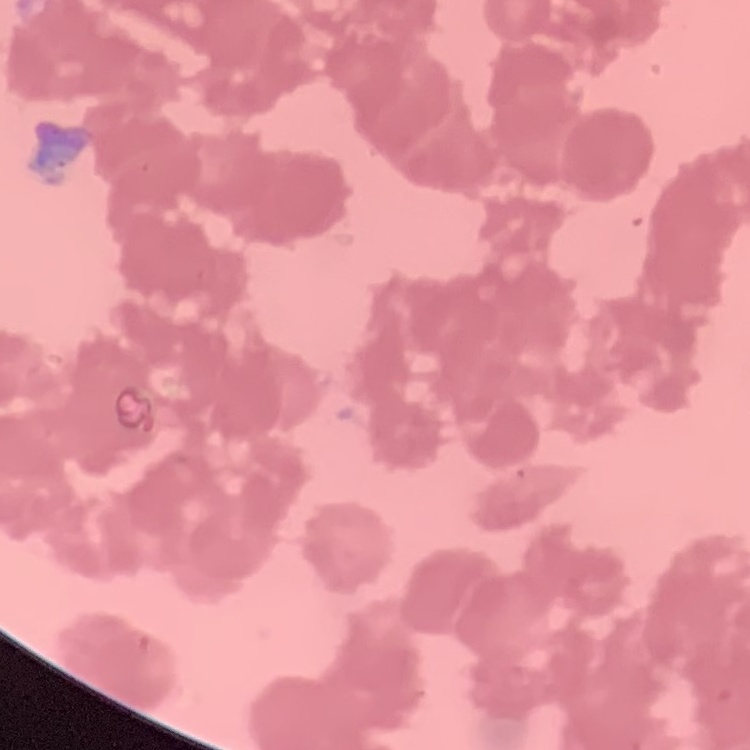
The red blood cells exhibit rouleaux formation. One tile cut from a larger photomicrograph. Thin peripheral smear. Stained with either Field's or Giemsa.